Locate and identify every blood parasite.
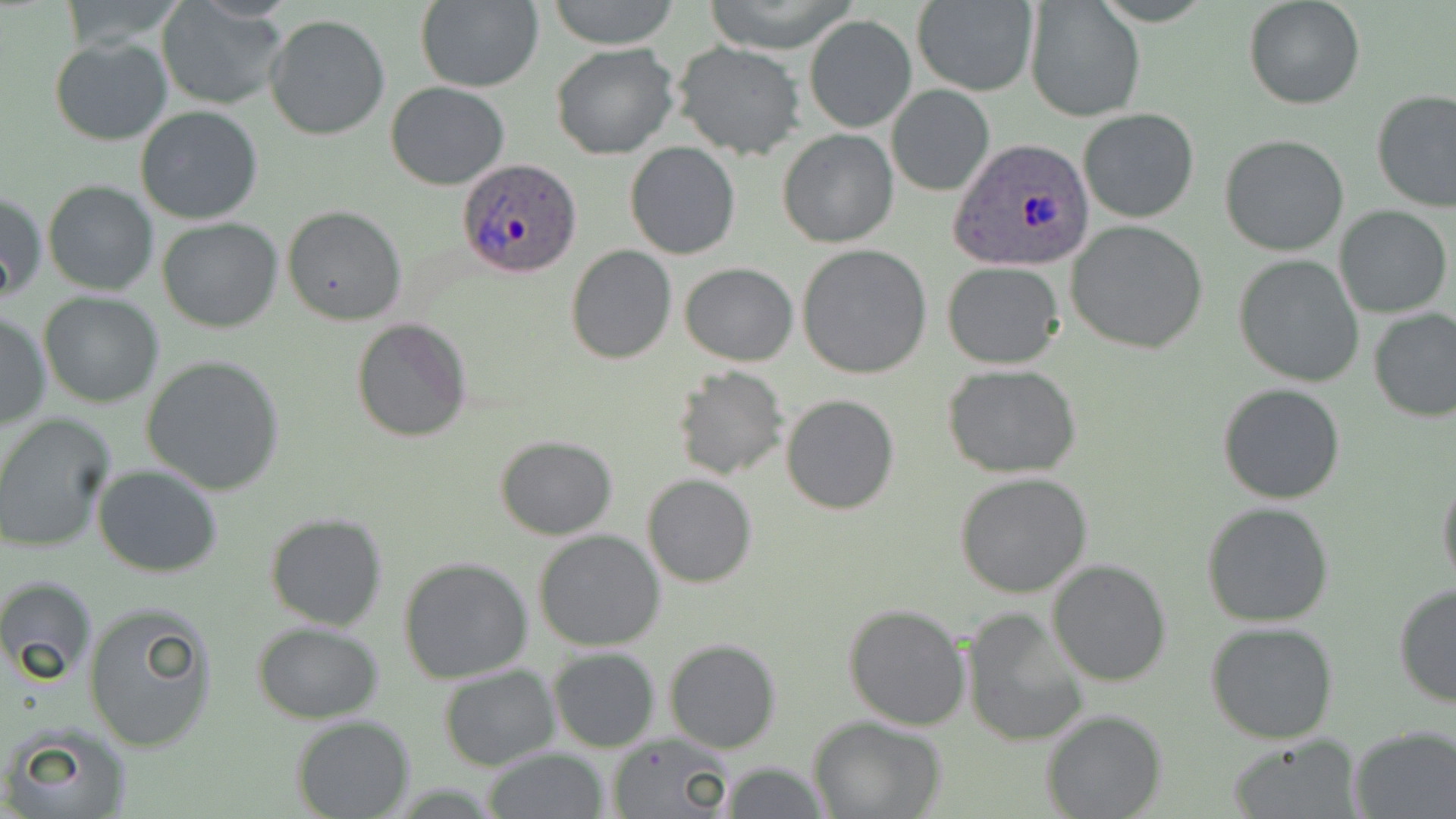
Approximate bounding boxes as named x1/y1/x2/y2 corners in pixels.
Plasmodium ovale-infected red blood cells: (x1=951, y1=136, x2=1093, y2=272), (x1=456, y1=158, x2=583, y2=279).
No Plasmodium falciparum, Plasmodium malariae, Plasmodium vivax, Babesia divergens, or Trypanosoma brucei observed.

Summary:
  - Uninfected red blood cell locations: (x1=59, y1=0, x2=185, y2=53), (x1=414, y1=0, x2=544, y2=92), (x1=544, y1=0, x2=682, y2=49), (x1=700, y1=0, x2=863, y2=55), (x1=1242, y1=0, x2=1367, y2=110), (x1=155, y1=1, x2=288, y2=111), (x1=1025, y1=1, x2=1144, y2=121), (x1=910, y1=2, x2=1038, y2=97), (x1=805, y1=14, x2=916, y2=134), (x1=263, y1=15, x2=390, y2=141), (x1=50, y1=37, x2=174, y2=146), (x1=673, y1=42, x2=806, y2=162), (x1=551, y1=43, x2=678, y2=159), (x1=384, y1=82, x2=510, y2=189), (x1=886, y1=84, x2=994, y2=197), (x1=1371, y1=90, x2=1456, y2=211), (x1=135, y1=105, x2=264, y2=225), (x1=1077, y1=108, x2=1199, y2=225), (x1=778, y1=127, x2=898, y2=248), (x1=1219, y1=134, x2=1350, y2=256), (x1=625, y1=142, x2=740, y2=259), (x1=44, y1=180, x2=158, y2=296), (x1=1, y1=191, x2=46, y2=303), (x1=283, y1=205, x2=406, y2=326), (x1=1334, y1=205, x2=1453, y2=317), (x1=157, y1=218, x2=283, y2=333), (x1=1067, y1=220, x2=1209, y2=354), (x1=797, y1=245, x2=933, y2=379), (x1=567, y1=246, x2=677, y2=363), (x1=1233, y1=255, x2=1365, y2=389), (x1=942, y1=261, x2=1063, y2=370), (x1=680, y1=263, x2=798, y2=365), (x1=39, y1=292, x2=164, y2=407), (x1=1369, y1=307, x2=1456, y2=421), (x1=0, y1=310, x2=51, y2=432), (x1=351, y1=317, x2=472, y2=442), (x1=142, y1=354, x2=286, y2=496), (x1=672, y1=365, x2=788, y2=481), (x1=943, y1=365, x2=1082, y2=478), (x1=1217, y1=382, x2=1347, y2=504), (x1=781, y1=393, x2=899, y2=514), (x1=0, y1=414, x2=114, y2=552), (x1=495, y1=435, x2=619, y2=540), (x1=93, y1=464, x2=223, y2=579), (x1=1437, y1=468, x2=1456, y2=596), (x1=953, y1=472, x2=1093, y2=597), (x1=642, y1=474, x2=758, y2=588), (x1=1201, y1=502, x2=1335, y2=628), (x1=264, y1=512, x2=389, y2=631), (x1=533, y1=530, x2=665, y2=651), (x1=397, y1=557, x2=534, y2=682), (x1=1047, y1=560, x2=1174, y2=686), (x1=0, y1=575, x2=98, y2=686), (x1=1392, y1=584, x2=1456, y2=707), (x1=83, y1=601, x2=217, y2=754), (x1=842, y1=604, x2=970, y2=731), (x1=964, y1=608, x2=1091, y2=745), (x1=251, y1=621, x2=384, y2=723), (x1=1204, y1=622, x2=1339, y2=744), (x1=663, y1=639, x2=781, y2=753), (x1=548, y1=648, x2=660, y2=752), (x1=439, y1=666, x2=560, y2=770), (x1=1041, y1=707, x2=1166, y2=818), (x1=290, y1=715, x2=415, y2=819), (x1=809, y1=716, x2=950, y2=819), (x1=4, y1=719, x2=134, y2=819), (x1=1349, y1=726, x2=1456, y2=818), (x1=606, y1=734, x2=735, y2=818), (x1=1228, y1=735, x2=1363, y2=818), (x1=481, y1=747, x2=609, y2=819), (x1=718, y1=761, x2=830, y2=818)
  - Slide-level diagnosis: Plasmodium ovale
  - Preparation: thin blood smear
  - Modality: optical microscopy
  - Stain: May-Grünwald-Giemsa
  - Image size: 1456×819 pixels
  - Field of view: single
  - Magnification: 1000x